Name the parasite shown.
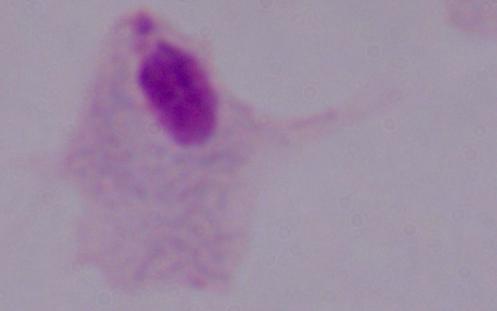

A trichomonad.

modality: micrograph
magnification: 1000x